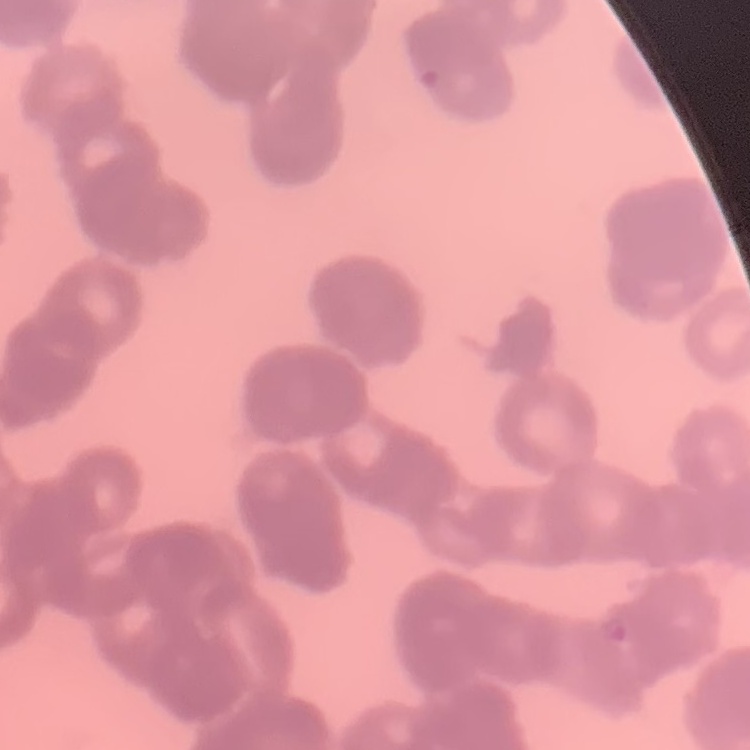

Summary:
  - Red blood cell morphology: rouleaux formation
  - Image type: one tile cut from a larger photomicrograph
  - Stain: Field's or Giemsa
  - Preparation: thin blood film